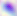
{
  "magnification": "400x",
  "identification": "Toxoplasma gondii",
  "modality": "micrograph"
}